Assess this cell for malaria.
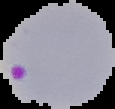

Parasitized.

Summary:
  - Image size: 115×109 pixels
  - Image type: segmented cell region with the area outside set to black
  - Preparation: thin blood smear